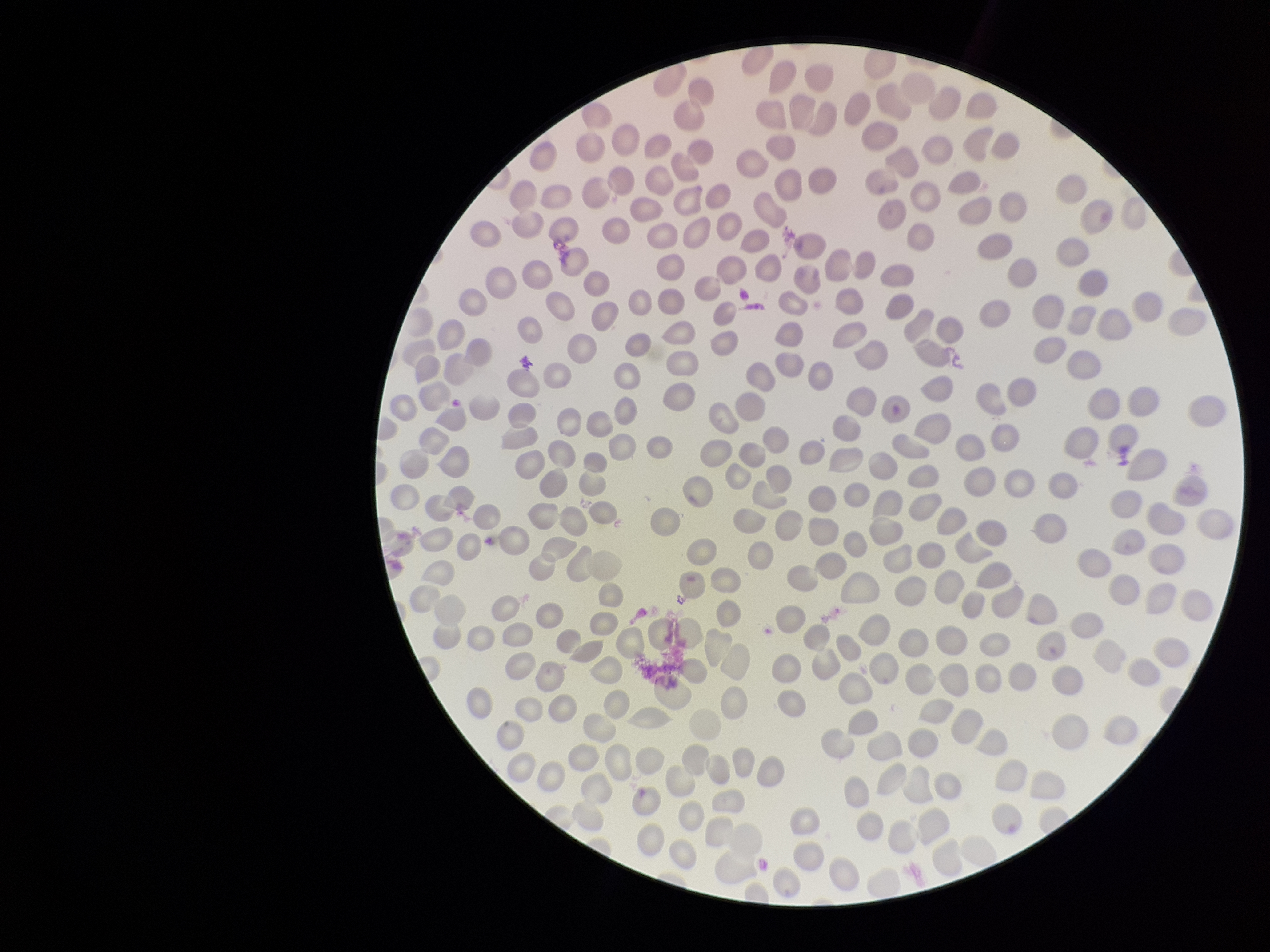

Patient malaria status: negative. Image is 1270×952 pixels. Preparation: thin. Photographed through the microscope eyepiece with a smartphone camera. Red blood cell count: 278. Single field of view. Giemsa stain. Parasitized red blood cell count: 0. Parasitized red blood cells: none detected.